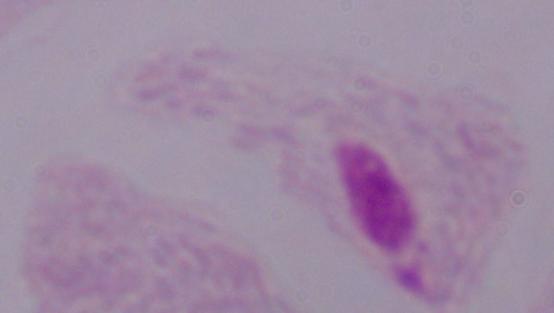

Summary:
  - Modality: micrograph
  - Magnification: 1000x
  - Identification: trichomonad